Classify this cell by malaria status.
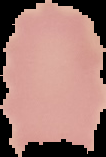

Uninfected.

image_size: 106×157 pixels
preparation: thin blood film
image_type: segmented cell region with the area outside set to black